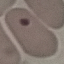

result = no malaria parasites detected
preparation = thin smear
capture = smartphone camera at the microscope eyepiece
image type = automatically extracted cell patch, resized to 64 × 64 pixels
stain = Giemsa